Assess the morphology of the red blood cells.
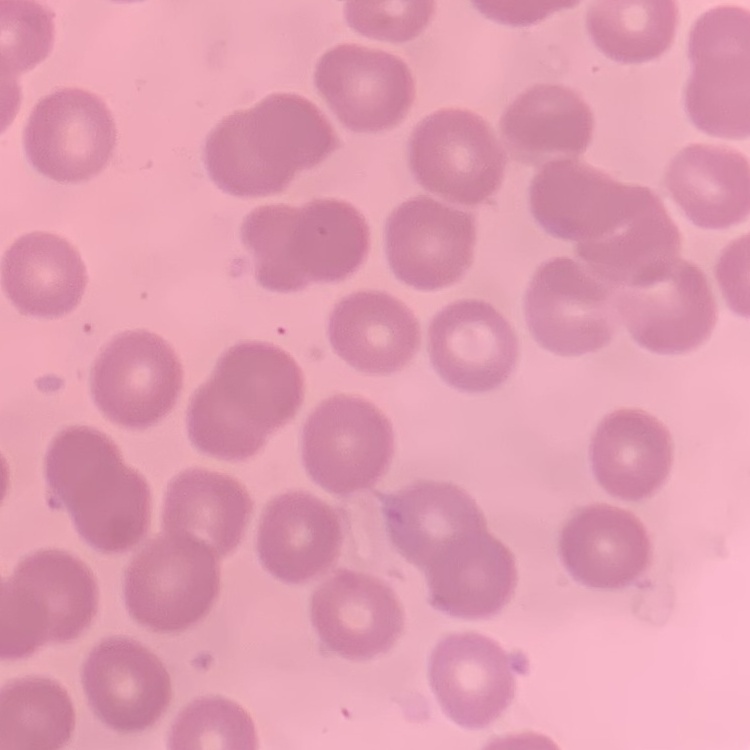

They show no rouleaux formation.

image_type: square crop of a larger photomicrograph
preparation: thin peripheral smear
stain: Field's or Giemsa